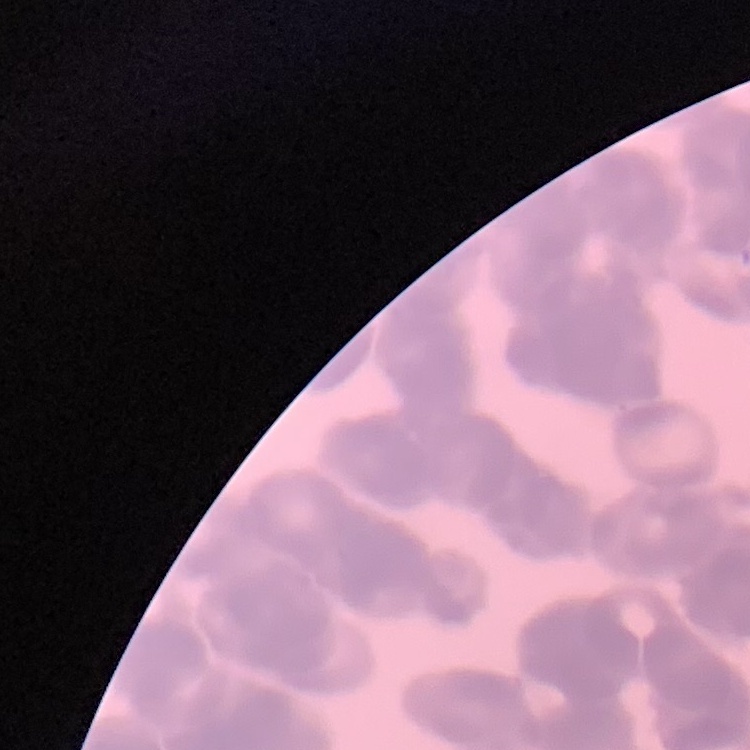

Summary:
  - Red blood cell morphology: rouleaux formation
  - Preparation: thin blood smear
  - Image type: square crop of a larger photomicrograph
  - Stain: Field's or Giemsa